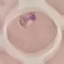
Summary:
  - Malaria status: parasitized
  - Capture: smartphone camera at the microscope eyepiece
  - Preparation: thin blood film
  - Image type: automatically extracted cell patch, resized to 64 × 64 pixels
  - Stain: Giemsa